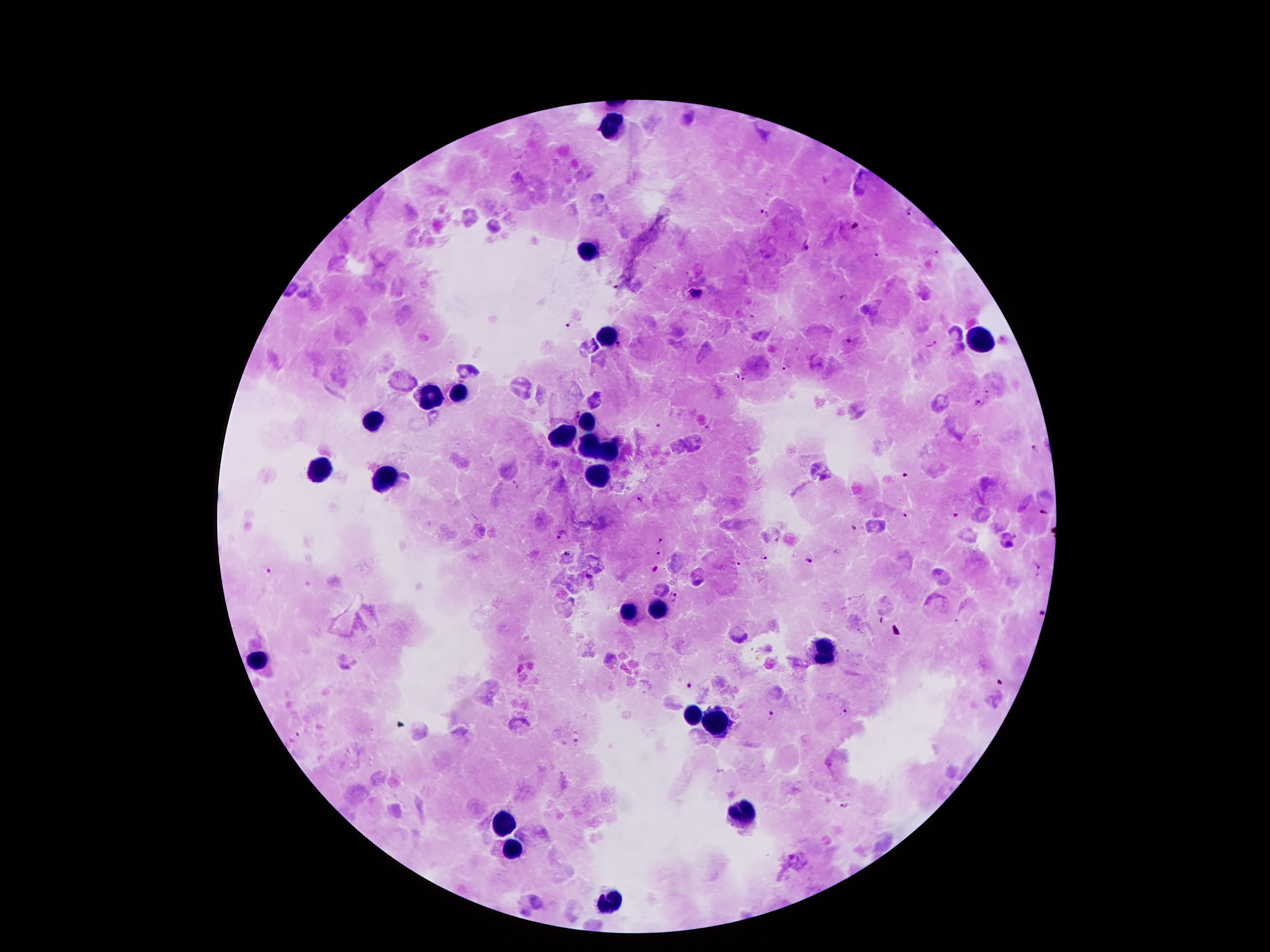

Approximate centers as [x, y] in pixels.
Summary:
  - Leukocyte locations: [612, 128], [587, 252], [608, 332], [980, 342], [459, 393], [428, 399], [587, 418], [369, 420], [562, 437], [587, 445], [608, 454], [318, 472], [598, 475], [385, 477], [656, 609], [625, 611], [826, 653], [257, 661], [694, 714], [719, 724], [742, 813], [501, 825], [511, 851], [606, 901]
  - Malaria parasite locations: [764, 212], [909, 212], [854, 222], [806, 248], [937, 250], [875, 255], [617, 287], [695, 295], [569, 326], [618, 344], [930, 345], [786, 368], [734, 375], [745, 380], [987, 393], [976, 404], [658, 426], [708, 426], [1034, 446], [904, 476], [639, 500], [1042, 513], [904, 515], [954, 515], [852, 529], [563, 534], [660, 541], [658, 552], [568, 553], [762, 558], [809, 561], [737, 563], [653, 569], [1040, 570], [267, 571], [673, 596], [1040, 612], [692, 683], [845, 711], [772, 716], [297, 737], [577, 740], [846, 805]
  - Field of view: single
  - Capture: smartphone camera through the microscope eyepiece
  - Preparation: thick blood smear
  - Stain: Giemsa
  - Patient malaria status: positive for Plasmodium falciparum
  - Magnification: 100x
  - Image size: 1270×952 pixels